Give the position of every leukocyte visible.
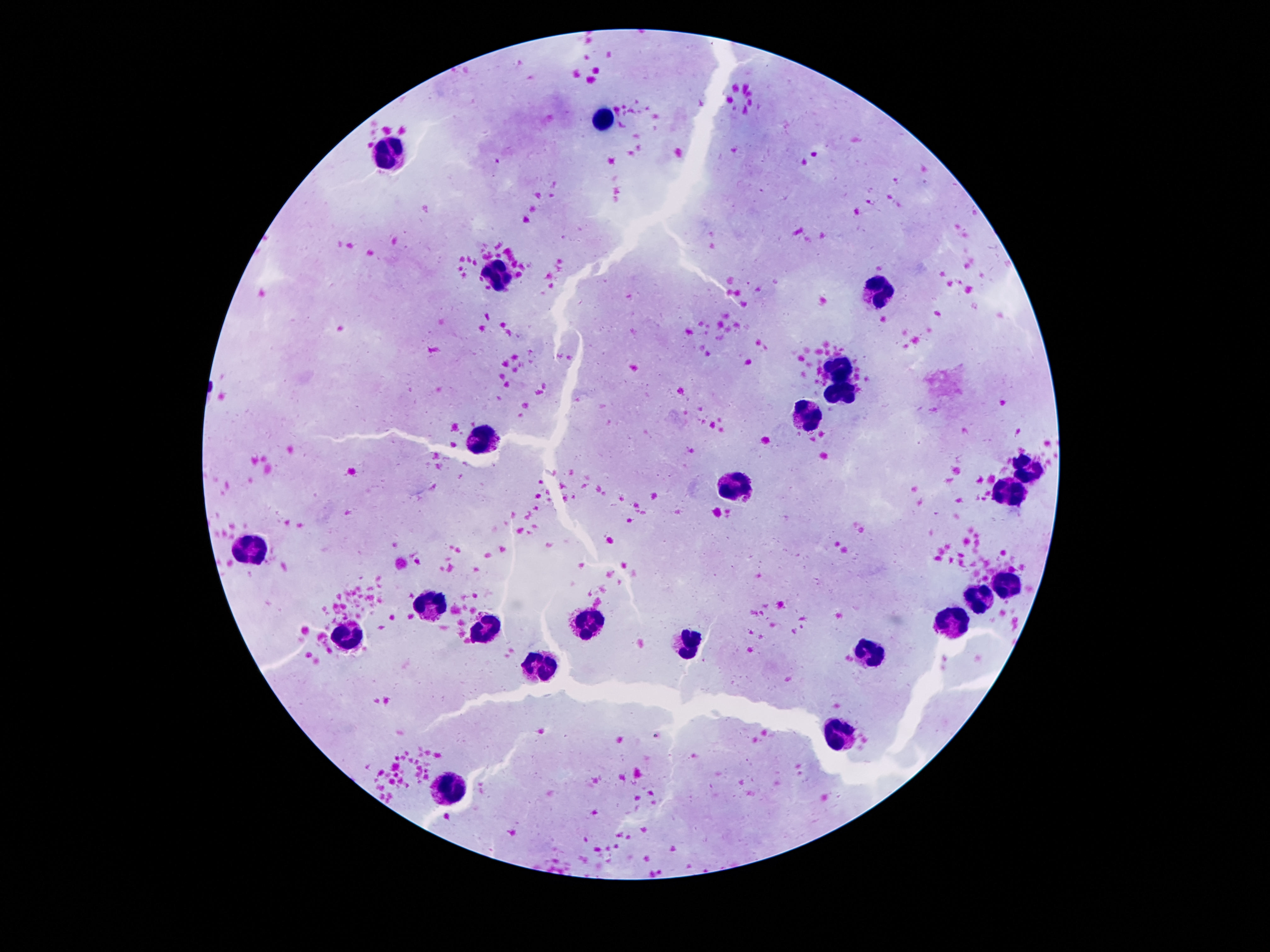

Approximate centers as {x, y} in pixels.
Leukocytes: {598, 119}, {391, 150}, {501, 277}, {881, 290}, {837, 365}, {842, 394}, {811, 418}, {483, 438}, {1031, 469}, {733, 488}, {1012, 489}, {253, 547}, {1012, 586}, {979, 600}, {433, 608}, {587, 622}, {954, 624}, {488, 627}, {342, 635}, {691, 642}, {873, 653}, {541, 664}, {842, 735}, {453, 788}.

Photographed through the microscope eyepiece with a smartphone camera. Single field of view. Giemsa-stained preparation. Patient malaria status: not infected. 100x magnification. Thick peripheral-blood smear. Image is 1270×952 pixels.